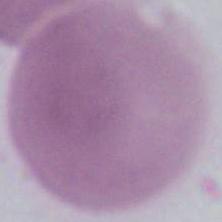

magnification = 1000x
modality = micrograph
identification = erythrocyte